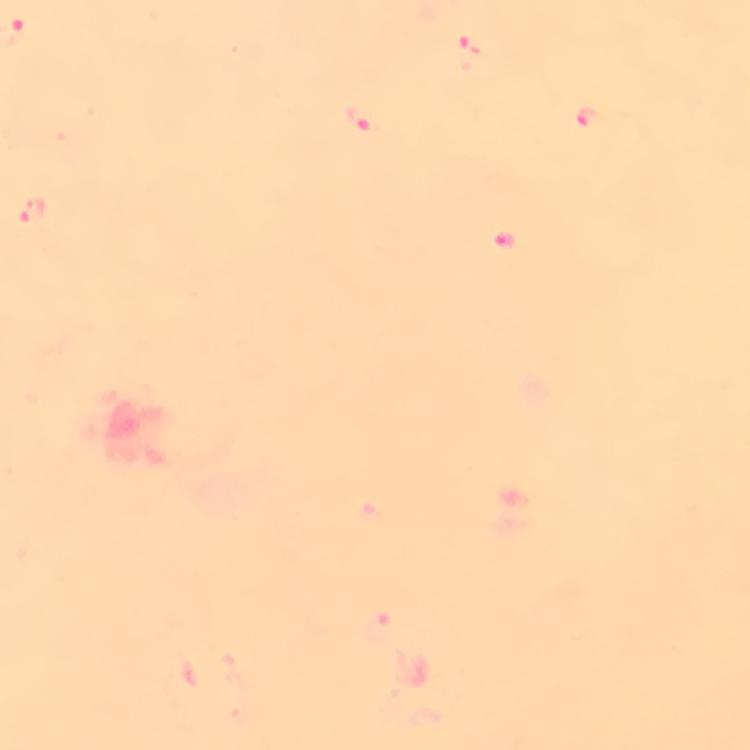
Approximate object centers, in pixels from the top-left corner.
Summary:
  - Malaria parasite locations: (x=465, y=53), (x=589, y=117), (x=364, y=119), (x=35, y=210), (x=382, y=630)
  - Capture: smartphone camera through the microscope
  - Magnification: 100x
  - Context: from a diagnostic examination for malaria
  - Stain: Giemsa
  - Preparation: thick blood smear
  - Image size: 750×750 pixels
  - Immersion oil: applied
  - Cropped from: a single field of view